Classify this cell by malaria status.
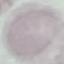

It is uninfected.

Summary:
  - Stain: Giemsa
  - Capture: smartphone through the microscope eyepiece
  - Preparation: thin smear
  - Image type: cell patch, automatically extracted from a larger field of view and resized to 64 × 64 pixels